Locate the cells, classifying each as a parasitized RBC, an uninfected RBC, or a WBC.
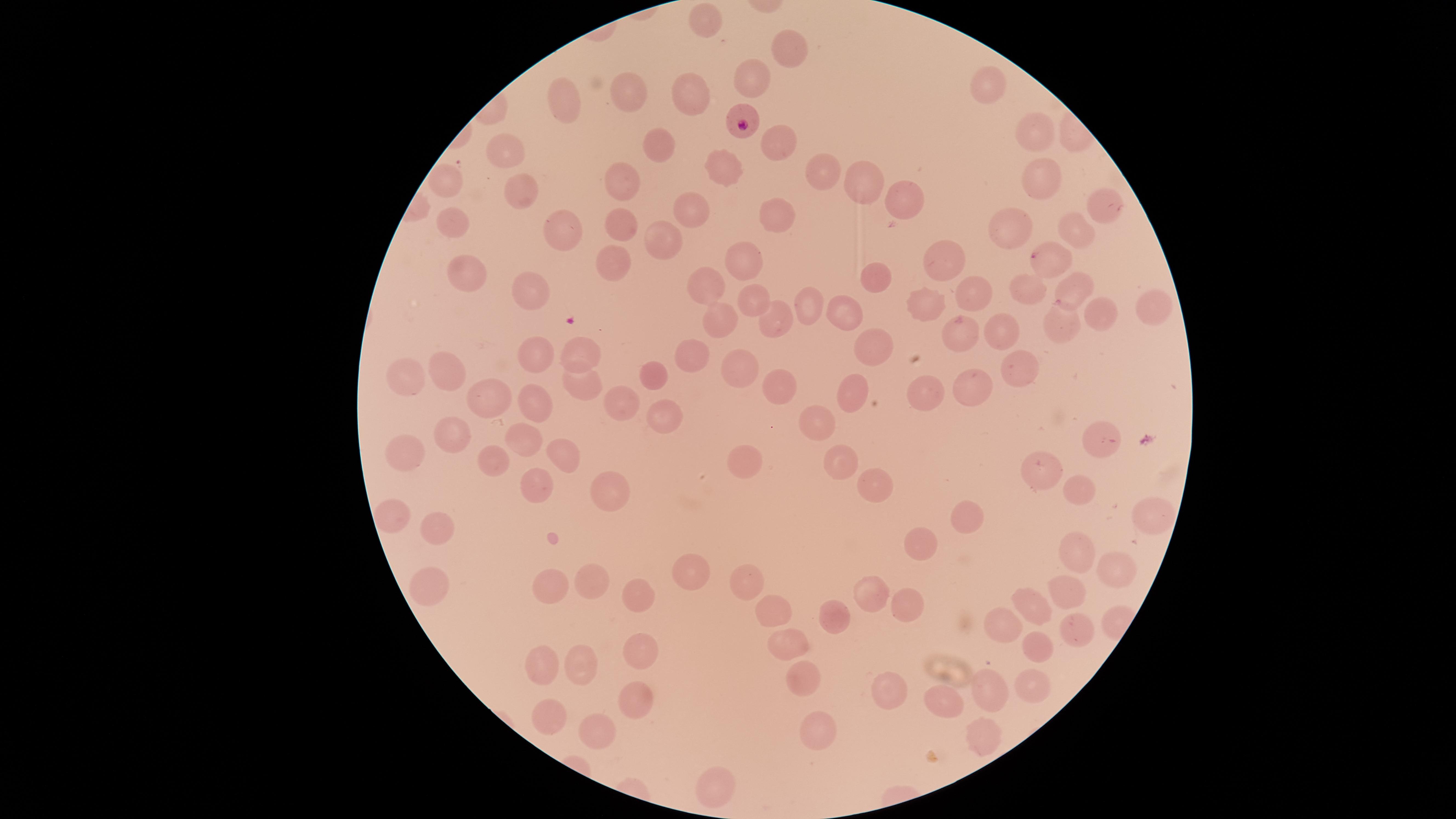

Approximate marker points as {x, y} in pixels.
Parasitized RBCs: {744, 121}, {1034, 255}.
Uninfected RBCs: {710, 24}, {789, 51}, {750, 80}, {990, 83}, {625, 88}, {696, 96}, {568, 104}, {1034, 131}, {776, 139}, {659, 146}, {507, 151}, {723, 169}, {821, 171}, {1038, 174}, {621, 182}, {866, 182}, {448, 184}, {522, 190}, {902, 196}, {1102, 207}, {690, 208}, {780, 217}, {457, 223}, {617, 223}, {1017, 227}, {558, 228}, {1075, 228}, {664, 238}, {943, 259}, {743, 261}, {466, 266}, {611, 268}, {880, 280}, {703, 284}, {531, 286}, {1079, 286}, {1030, 288}, {976, 293}, {751, 297}, {804, 300}, {932, 304}, {1147, 306}, {846, 312}, {721, 313}, {1096, 315}, {770, 325}, {1060, 326}, {998, 329}, {961, 333}, {873, 344}, {687, 345}, {535, 352}, {575, 354}, {1017, 361}, {743, 364}, {448, 367}, {657, 370}, {403, 376}, {971, 383}, {580, 386}, {776, 388}, {854, 392}, {489, 395}, {931, 395}, {536, 405}, {621, 406}, {662, 413}, {820, 419}, {1094, 435}, {457, 438}, {526, 440}, {404, 452}, {558, 452}, {499, 458}, {842, 460}, {744, 465}, {1042, 472}, {875, 484}, {534, 487}, {1069, 489}, {608, 491}, {396, 513}, {966, 514}, {1145, 516}, {433, 528}, {923, 541}, {1076, 553}, {1113, 560}, {687, 575}, {593, 579}, {557, 581}, {428, 582}, {745, 588}, {866, 593}, {1067, 593}, {637, 596}, {904, 603}, {1034, 603}, {772, 616}, {833, 619}, {1006, 624}, {1075, 629}, {1036, 644}, {789, 648}, {637, 650}, {545, 658}, {582, 661}, {801, 681}, {1033, 686}, {989, 688}, {894, 694}, {950, 699}, {633, 702}, {547, 717}, {595, 732}, {813, 732}, {981, 735}, {723, 781}.
No WBCs identified.

Summary:
  - Capture: smartphone photograph through the microscope eyepiece
  - Visible region: circular
  - Field of view: single
  - Preparation: thin blood smear
  - Stain: Giemsa
  - Species: Plasmodium falciparum
  - Image size: 1456×819 pixels